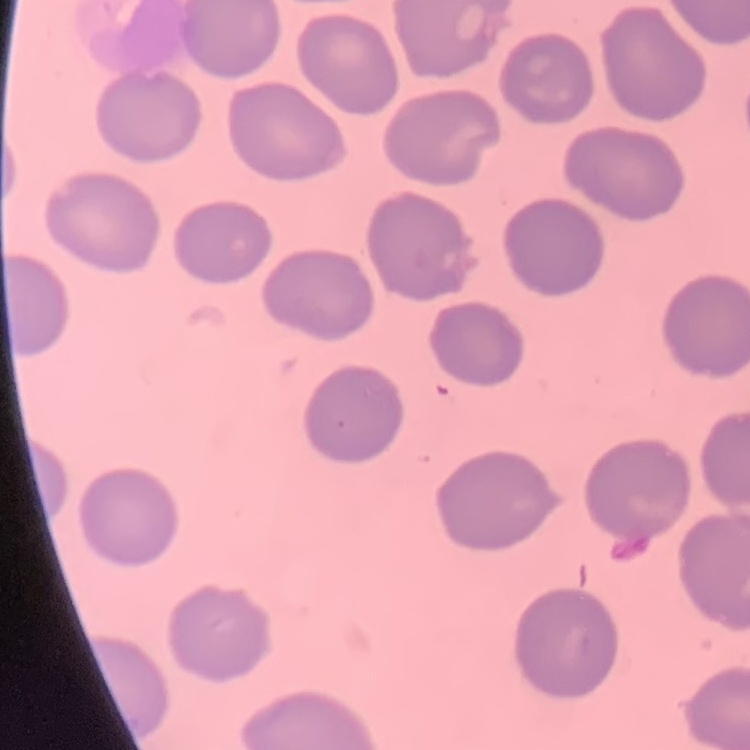 The erythrocytes show no rouleaux formation. One tile cut from a larger photomicrograph. Field's or Giemsa stain. Thin blood smear.